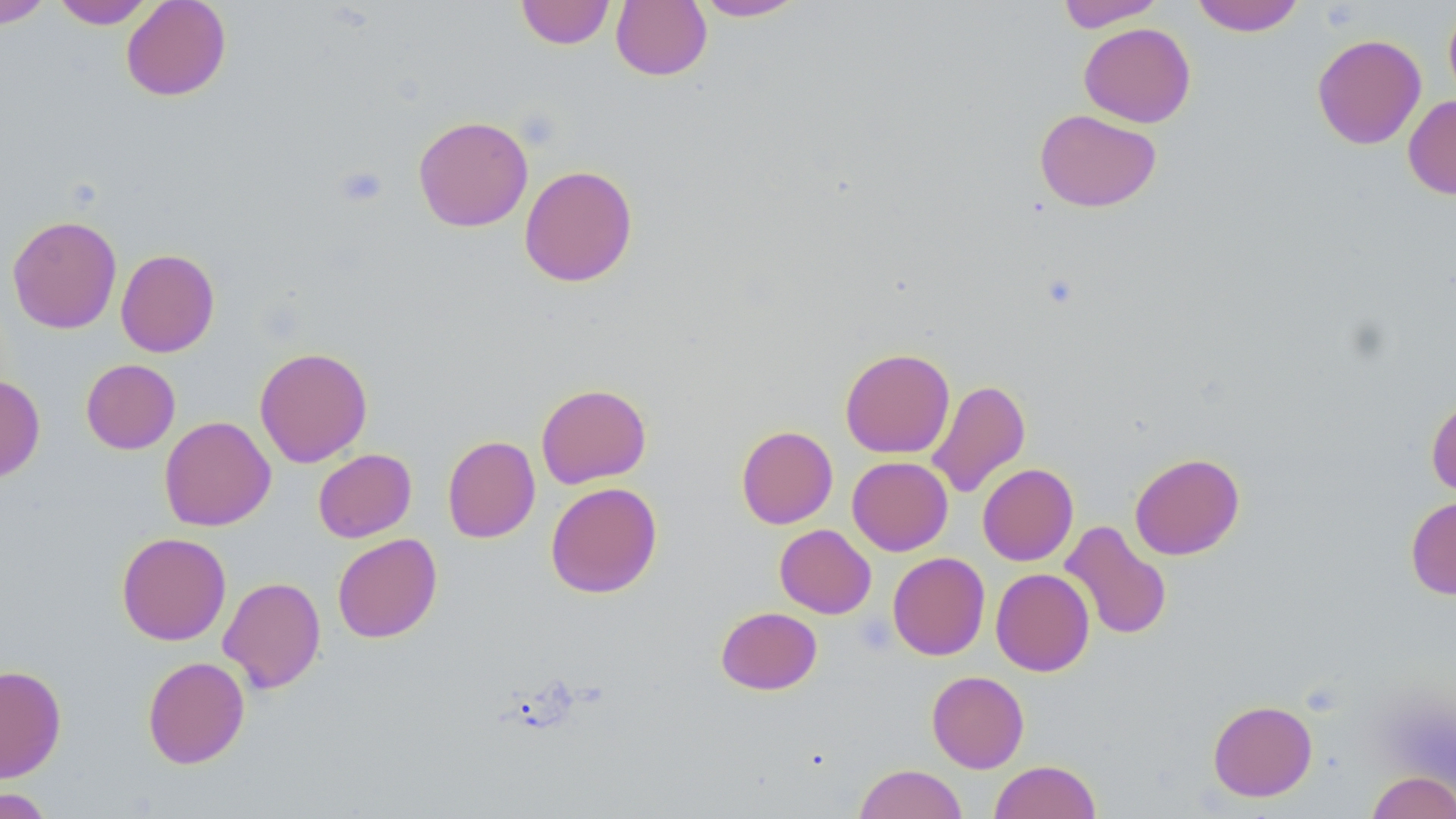
slide-level diagnosis = negative for blood parasites
platelet locations = approximate bounding boxes as named x1/y1/x2/y2 corners in pixels: (x1=335, y1=165, x2=389, y2=208)
image size = 1456×819 pixels
field of view = single
uninfected red blood cell locations = approximate bounding boxes as named x1/y1/x2/y2 corners in pixels: (x1=0, y1=0, x2=53, y2=28), (x1=51, y1=0, x2=157, y2=29), (x1=121, y1=0, x2=231, y2=101), (x1=516, y1=0, x2=614, y2=49), (x1=693, y1=0, x2=808, y2=21), (x1=1055, y1=0, x2=1165, y2=31), (x1=1190, y1=0, x2=1306, y2=36), (x1=611, y1=1, x2=712, y2=81), (x1=1444, y1=4, x2=1456, y2=106), (x1=1079, y1=22, x2=1196, y2=127), (x1=1312, y1=33, x2=1427, y2=150), (x1=1403, y1=95, x2=1456, y2=199), (x1=1034, y1=108, x2=1162, y2=212), (x1=413, y1=115, x2=533, y2=232), (x1=519, y1=165, x2=638, y2=287), (x1=7, y1=215, x2=122, y2=334), (x1=115, y1=249, x2=219, y2=357), (x1=254, y1=346, x2=373, y2=467), (x1=840, y1=348, x2=955, y2=458), (x1=81, y1=359, x2=180, y2=454), (x1=0, y1=374, x2=45, y2=482), (x1=927, y1=379, x2=1030, y2=499), (x1=535, y1=383, x2=652, y2=489), (x1=1426, y1=396, x2=1456, y2=498), (x1=159, y1=415, x2=276, y2=531), (x1=736, y1=425, x2=838, y2=529), (x1=442, y1=435, x2=540, y2=543), (x1=313, y1=449, x2=416, y2=542), (x1=1129, y1=452, x2=1245, y2=560), (x1=847, y1=456, x2=953, y2=556), (x1=977, y1=463, x2=1078, y2=566), (x1=545, y1=482, x2=662, y2=598), (x1=1405, y1=495, x2=1456, y2=600), (x1=1060, y1=521, x2=1172, y2=640), (x1=775, y1=524, x2=876, y2=619), (x1=116, y1=532, x2=231, y2=645), (x1=332, y1=533, x2=442, y2=643), (x1=888, y1=552, x2=990, y2=660), (x1=991, y1=568, x2=1094, y2=676), (x1=218, y1=576, x2=326, y2=693), (x1=716, y1=606, x2=822, y2=695), (x1=142, y1=656, x2=249, y2=769), (x1=0, y1=664, x2=67, y2=783), (x1=927, y1=670, x2=1029, y2=773), (x1=1208, y1=700, x2=1317, y2=801), (x1=989, y1=760, x2=1101, y2=819), (x1=854, y1=764, x2=967, y2=818), (x1=1366, y1=770, x2=1456, y2=819), (x1=1, y1=786, x2=57, y2=818)
modality = light microscopy
stain = May-Grünwald-Giemsa
preparation = thin blood smear
magnification = 1000x